Classify this cell by malaria status.
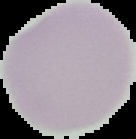

Uninfected.

Summary:
  - Preparation: thin blood film
  - Image type: segmented cell region on a black background
  - Image size: 136×139 pixels